Assess this cell for malaria.
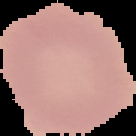
It is uninfected.

preparation = thin blood smear
image size = 136×136 pixels
image type = segmented cell region with the area outside set to black